Describe the morphology of the erythrocytes.
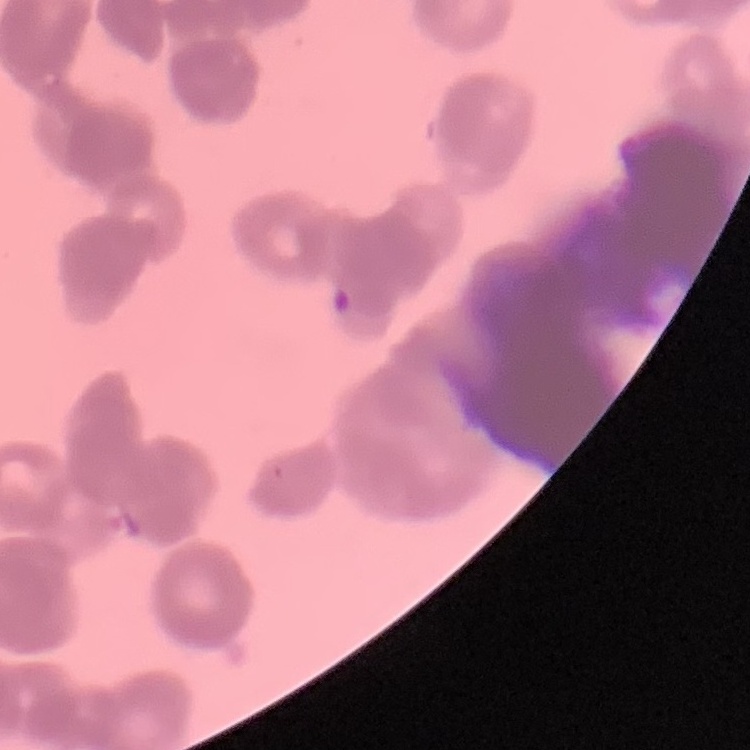
They show rouleaux formation.

preparation = thin blood film
stain = Field's or Giemsa
image type = square crop of a larger photomicrograph